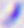

magnification: 400x
identification: Toxoplasma gondii
modality: micrograph